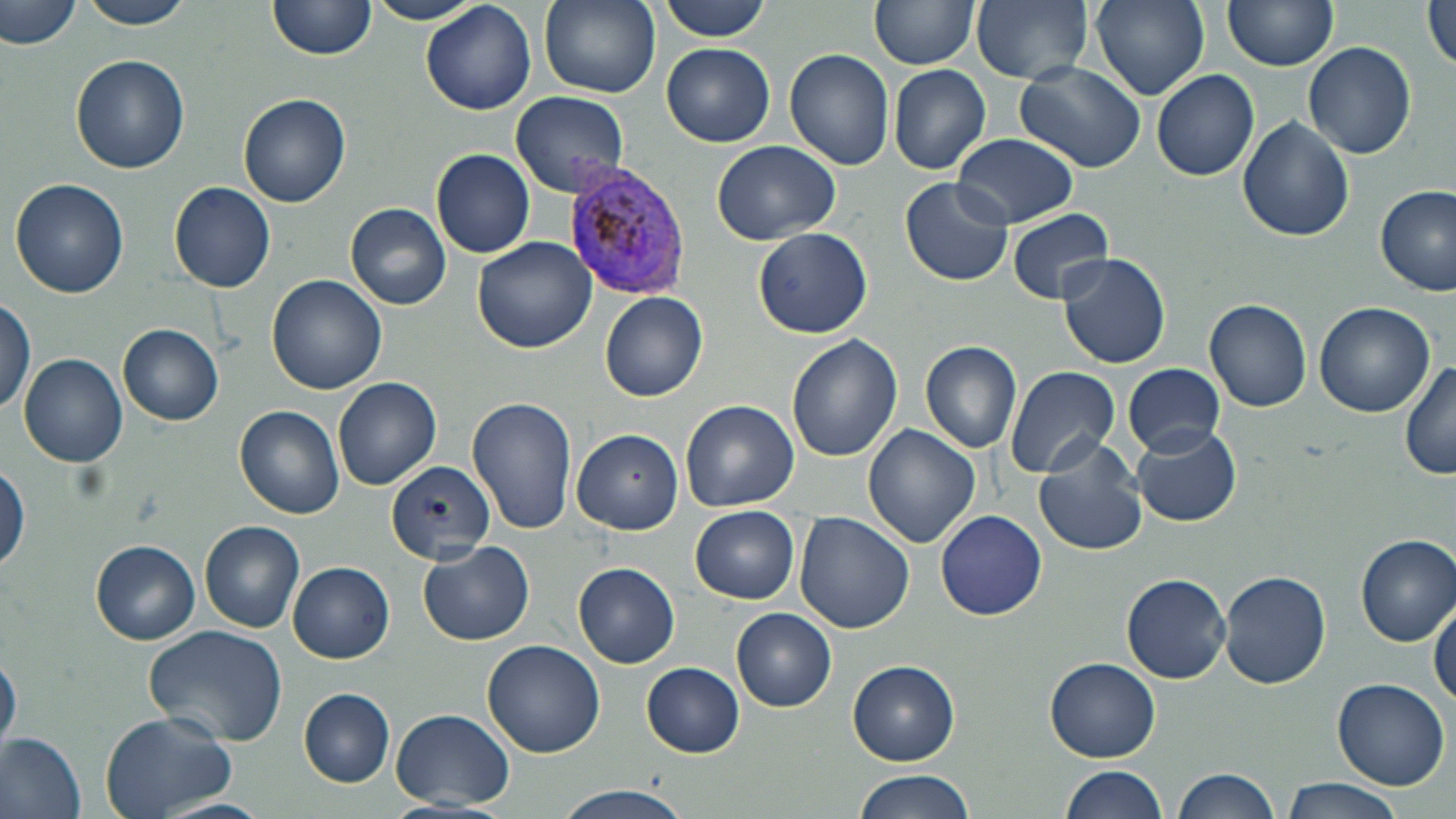

Summary:
  - Coordinate format: approximate bounding boxes as (x1,y1)-(x2,y2) corner pairs in pixels
  - Uninfected red blood cell locations: (73,0)-(199,28), (268,0)-(377,59), (363,0)-(483,25), (538,0)-(662,99), (657,0)-(773,41), (870,0)-(978,70), (971,0)-(1094,84), (1089,0)-(1211,99), (1223,0)-(1339,71), (1,1)-(83,50), (422,1)-(537,116), (1422,3)-(1456,75), (1302,41)-(1415,160), (663,42)-(775,146), (785,48)-(896,171), (71,54)-(190,173), (1014,62)-(1145,172), (887,64)-(991,175), (1151,68)-(1260,182), (510,90)-(631,198), (237,94)-(351,208), (1238,116)-(1356,242), (953,132)-(1079,229), (711,140)-(842,244), (432,149)-(536,257), (900,176)-(1014,288), (9,178)-(129,299), (169,182)-(278,293), (1375,184)-(1454,298), (345,202)-(451,310), (1005,206)-(1115,306), (752,227)-(873,339), (473,237)-(597,352), (1058,251)-(1171,369), (266,274)-(387,395), (600,292)-(709,402), (0,298)-(34,417), (1204,299)-(1312,412), (1315,302)-(1436,418), (118,324)-(224,425), (787,335)-(903,462), (919,341)-(1023,454), (19,352)-(128,467), (1400,358)-(1456,483), (1122,363)-(1225,457), (1003,365)-(1120,478), (334,376)-(442,490), (468,396)-(579,535), (681,399)-(799,512), (235,405)-(346,518), (863,424)-(980,548), (1131,427)-(1242,527), (571,428)-(683,535), (1033,438)-(1149,556), (386,460)-(496,563), (0,463)-(28,577), (690,506)-(800,604), (935,509)-(1048,620), (795,513)-(914,633), (200,522)-(304,634), (1356,535)-(1456,646), (89,539)-(200,644), (418,540)-(534,646), (288,562)-(394,663), (573,562)-(680,668), (1219,570)-(1332,688), (1121,573)-(1231,683), (1430,595)-(1456,708), (731,608)-(837,712), (144,625)-(291,750), (482,639)-(605,758), (0,649)-(21,758), (1046,658)-(1159,760), (849,659)-(961,764), (642,662)-(746,758), (1333,676)-(1450,789), (300,690)-(395,786), (392,708)-(514,809), (100,711)-(241,819), (1,733)-(87,818), (1058,764)-(1167,819), (1170,767)-(1280,818), (851,770)-(973,819), (1278,781)-(1402,819), (552,784)-(695,819), (152,797)-(271,819)
  - Plasmodium vivax-infected red blood cell locations: (560,162)-(692,297)
  - Slide-level diagnosis: Plasmodium vivax
  - Image size: 1456×819 pixels
  - Preparation: thin blood smear
  - Modality: optical microscopy
  - Field of view: single
  - Stain: May-Grünwald-Giemsa
  - Magnification: 1000x